Name the parasite shown.
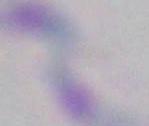
Toxoplasma gondii.

magnification = 1000x
modality = micrograph